Identify the parasite.
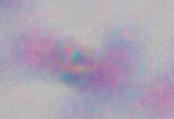

This is Toxoplasma gondii.

Summary:
  - Modality: micrograph
  - Magnification: 1000x